Name the parasite shown.
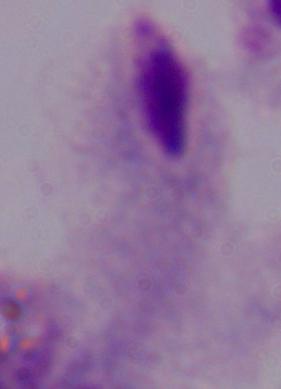

This is a trichomonad.

magnification = 1000x
modality = photomicrograph